Classify this cell by malaria status.
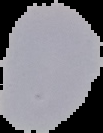
It is uninfected.

Image is 103×133 pixels. From a thin blood smear. The area outside the segmented cell region is set to black.